Name the parasite shown.
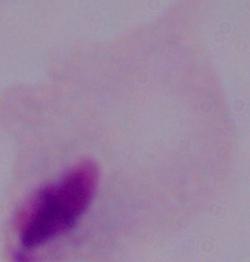
This is a trichomonad.

Summary:
  - Modality: micrograph
  - Magnification: 1000x